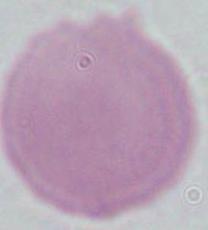
modality: photomicrograph
identification: erythrocyte
magnification: 1000x